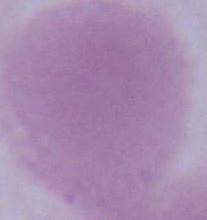
{
  "identification": "red blood cell",
  "magnification": "1000x",
  "modality": "photomicrograph"
}